Assess this cell for malaria.
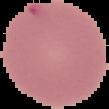

Uninfected.

Segmented cell region on a black background. Image is 109×109 pixels. From a thin blood smear.